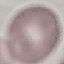
result = no malaria parasites seen
capture = smartphone through the microscope eyepiece
preparation = thin blood smear
image type = automatically extracted cell patch, resized to 64 × 64 pixels
stain = Giemsa